Name the parasite shown.
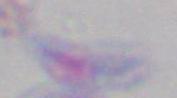

This is Toxoplasma gondii.

Summary:
  - Magnification: 1000x
  - Modality: photomicrograph